Give the position of each Plasmodium falciparum parasite with its life-cycle stage, each leukocyte, and any debris.
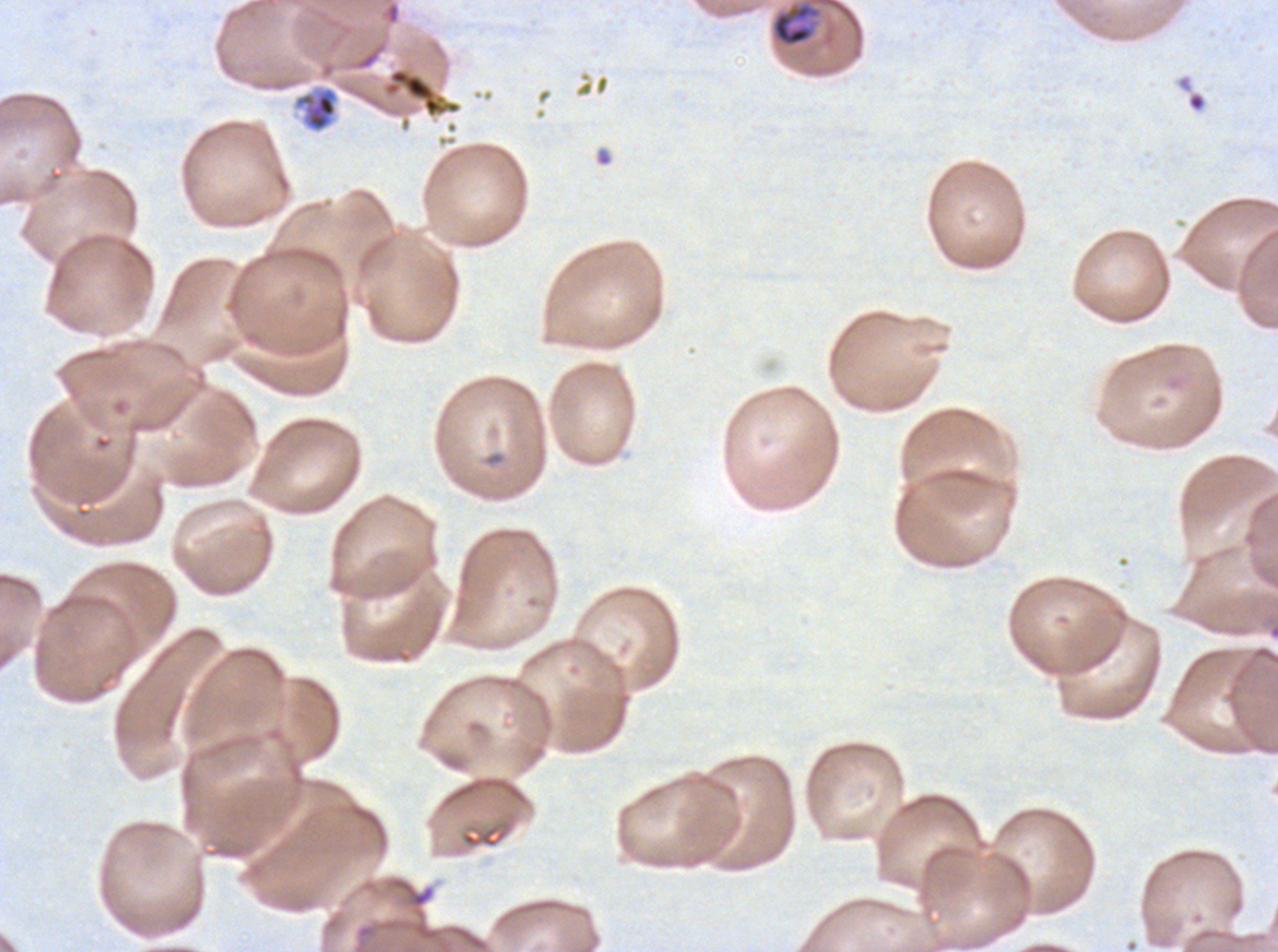

Approximate bounding rectangles given as corner coordinates in pixels from the top-left.
Mid trophozoites: (x1=770, y1=1, x2=821, y2=47).
Debris: (x1=384, y1=67, x2=461, y2=118), (x1=292, y1=85, x2=339, y2=133).
No rings, late-ring/early-trophozoite forms, late trophozoites, early schizonts, late schizonts, segmenters, gametocytes, or leukocytes observed.

Thin blood film. One sub-image of a larger composite. Plasmodium falciparum cultured ex vivo for 24 to 48 hours, from a patient in The Gambia. Image is 1278×952 pixels. Giemsa stain.